Locate every Plasmodium falciparum-infected red blood cell.
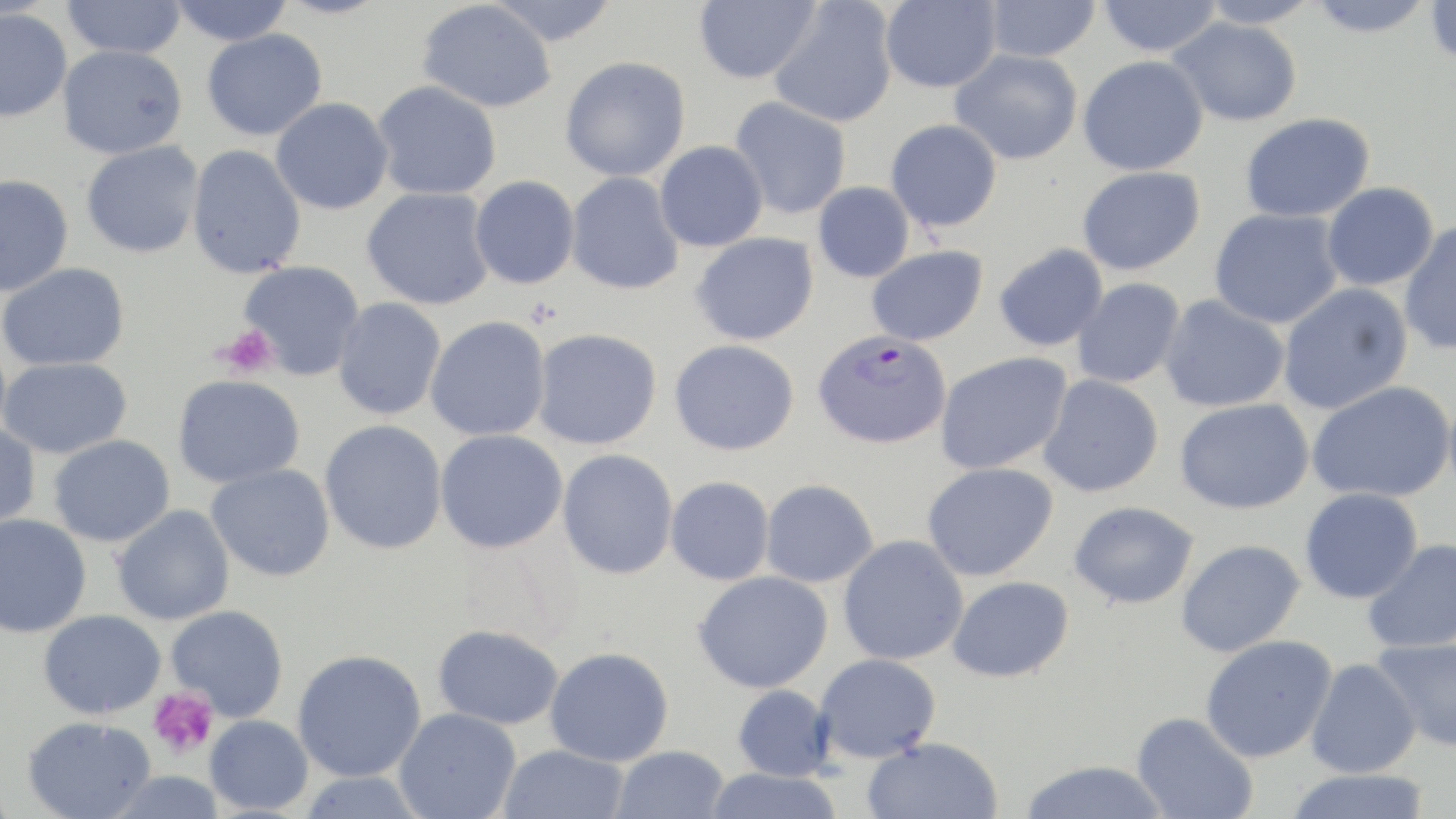
Approximate bounding boxes as [x1, y1, x2, y2] in pixels.
Plasmodium falciparum-infected red blood cells: [812, 329, 952, 449].

slide_level_diagnosis: Plasmodium falciparum
modality: optical microscopy
preparation: thin blood smear
stain: May-Grünwald-Giemsa
platelet_locations: 'approximate bounding boxes as [x1, y1, x2, y2] in pixels: [217, 324, 278, 379], [147, 687, 220, 760]'
field_of_view: single
uninfected_red_blood_cell_locations: 'approximate bounding boxes as [x1, y1, x2, y2] in pixels: [61, 0, 186, 59], [485, 0, 620, 47], [694, 0, 820, 84], [880, 0, 1001, 93], [983, 0, 1101, 63], [1098, 0, 1222, 57], [1195, 0, 1321, 28], [1305, 0, 1437, 37], [167, 1, 297, 45], [416, 1, 557, 113], [769, 1, 898, 127], [1425, 1, 1456, 68], [0, 8, 72, 122], [1168, 16, 1303, 126], [201, 28, 328, 141], [57, 44, 188, 159], [950, 49, 1083, 165], [560, 55, 691, 182], [1078, 55, 1208, 176], [372, 80, 502, 200], [730, 96, 852, 219], [270, 97, 394, 215], [1240, 112, 1375, 223], [885, 118, 1002, 232], [654, 140, 768, 252], [81, 141, 204, 259], [186, 144, 306, 278], [1077, 166, 1205, 275], [565, 172, 685, 295], [0, 174, 74, 296], [470, 175, 580, 289], [813, 181, 915, 282], [1321, 182, 1439, 291], [362, 187, 495, 310], [1209, 208, 1343, 329], [1399, 221, 1456, 356], [690, 232, 819, 346], [994, 243, 1108, 352], [866, 245, 988, 346], [238, 260, 365, 380], [0, 262, 130, 371], [1072, 278, 1185, 388], [1277, 283, 1413, 415], [1159, 294, 1290, 412], [333, 297, 446, 420], [425, 315, 551, 441], [532, 327, 662, 450], [670, 339, 800, 455], [935, 351, 1072, 474], [0, 357, 132, 459], [173, 374, 305, 488], [1038, 374, 1164, 497], [1305, 381, 1456, 504], [1174, 398, 1314, 515], [319, 419, 448, 555], [0, 423, 41, 531], [434, 429, 568, 554], [49, 434, 175, 547], [557, 448, 679, 579], [922, 462, 1058, 581], [206, 463, 335, 581], [665, 476, 774, 585], [760, 479, 879, 587], [1300, 487, 1423, 603], [1069, 500, 1200, 609], [112, 504, 235, 626], [0, 514, 92, 638], [838, 535, 969, 665], [1362, 538, 1456, 654], [1176, 539, 1305, 658], [693, 570, 833, 694], [947, 576, 1074, 682], [166, 605, 289, 721], [38, 609, 167, 718], [431, 624, 565, 729], [1200, 634, 1338, 763], [1372, 637, 1456, 752], [545, 646, 674, 766], [292, 649, 426, 782], [813, 653, 942, 763], [1305, 657, 1421, 778], [732, 684, 835, 782], [393, 707, 522, 819], [1131, 712, 1258, 819], [204, 714, 314, 815], [22, 716, 156, 819], [861, 736, 1004, 819], [497, 744, 629, 819], [610, 746, 730, 819], [1018, 759, 1171, 819], [702, 767, 843, 819], [1283, 769, 1432, 819], [104, 770, 226, 818], [296, 771, 428, 818]'
image_size: 1456×819 pixels
magnification: 1000x